Name the parasite shown.
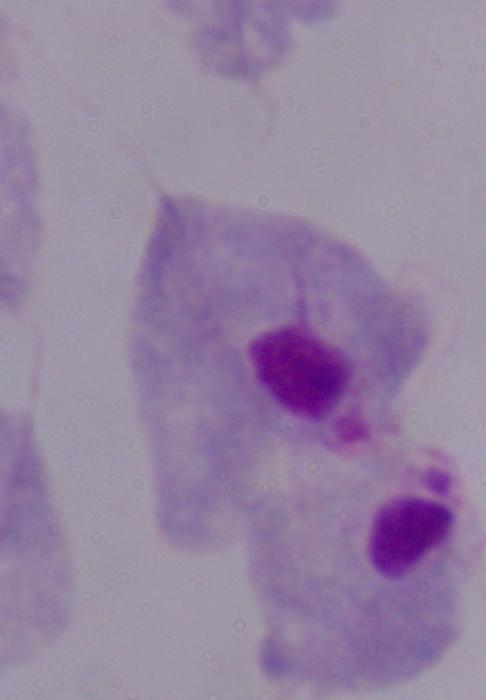
This is a trichomonad.

Summary:
  - Magnification: 1000x
  - Modality: photomicrograph